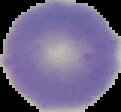

Summary:
  - Malaria status: uninfected
  - Preparation: thin blood smear
  - Image size: 121×112 pixels
  - Image type: segmented cell region on a black background